Assess the morphology of the red blood cells.
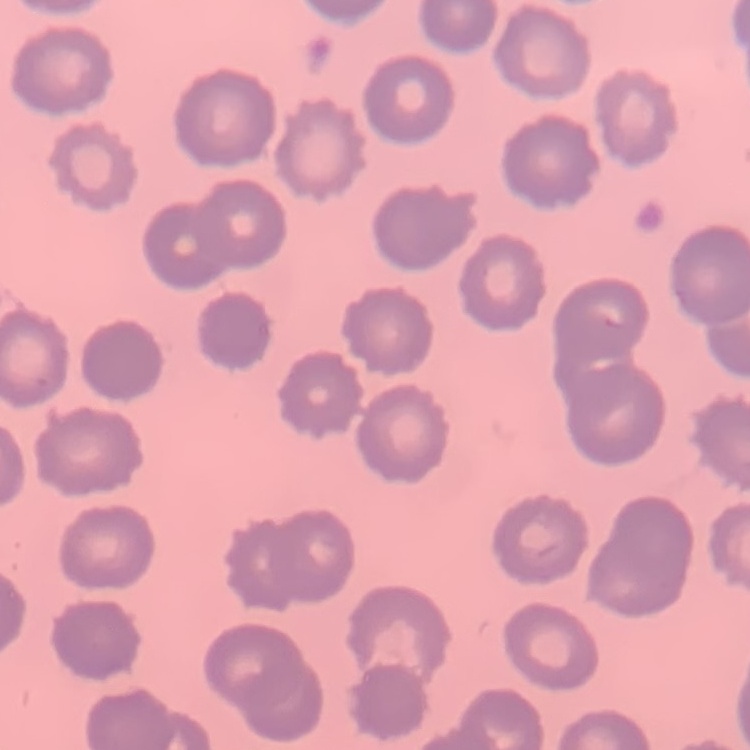
No rouleaux formation.

Summary:
  - Image type: square crop of a larger photomicrograph
  - Stain: Field's or Giemsa
  - Preparation: thin blood smear